Locate every uninfected red blood cell.
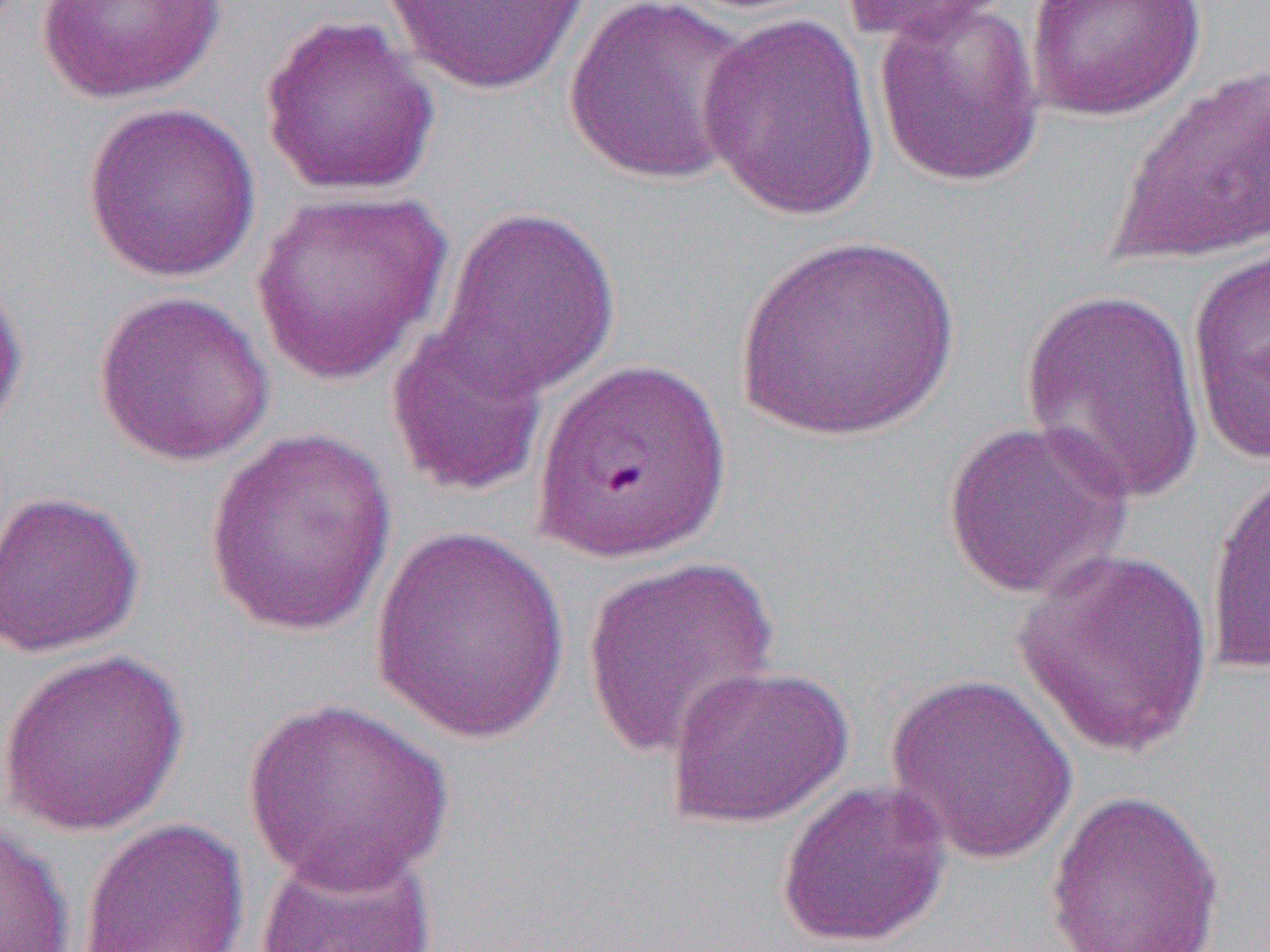

Approximate bounding boxes as (x1, y1, x2, y2) in pixels.
Uninfected red blood cells: (384, 0, 593, 96), (562, 0, 758, 187), (837, 0, 1020, 45), (1024, 0, 1207, 122), (34, 1, 228, 104), (872, 3, 1046, 188), (696, 12, 881, 222), (258, 13, 440, 197), (1106, 64, 1270, 269), (82, 102, 261, 283), (250, 188, 452, 385), (434, 206, 621, 401), (735, 234, 959, 440), (1186, 248, 1270, 466), (0, 258, 30, 442), (1018, 286, 1208, 508), (92, 289, 275, 467), (385, 318, 552, 499), (941, 417, 1133, 600), (204, 429, 398, 639), (1204, 467, 1270, 676), (0, 489, 145, 659), (369, 524, 570, 745), (1013, 545, 1216, 758), (583, 557, 779, 761), (0, 647, 191, 836), (664, 664, 853, 830), (884, 672, 1079, 865), (242, 696, 454, 892), (775, 779, 951, 949), (1043, 787, 1225, 952), (0, 817, 76, 952), (79, 817, 250, 952), (253, 842, 439, 952).

Slide-level diagnosis: Plasmodium falciparum. Thin blood smear. Image is 1270×952 pixels. Light microscopy. Captured at 1000x magnification. One field of a larger specimen.